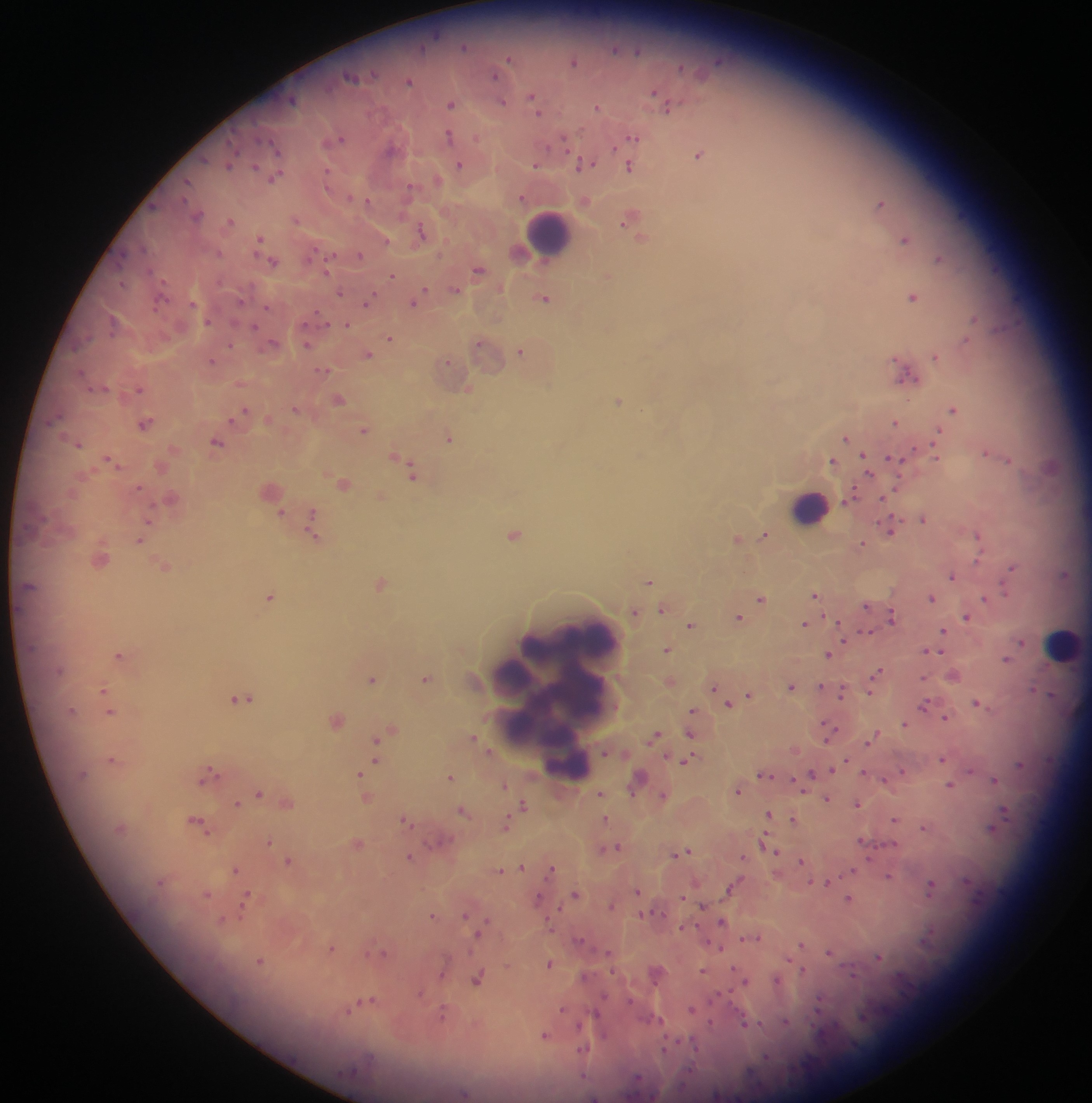

Approximate centers as {x, y} in pixels.
Summary:
  - Leukocyte locations: {549, 231}, {810, 505}, {570, 637}, {1062, 644}, {510, 680}, {559, 701}, {577, 702}, {567, 766}
  - Plasmodium parasite locations: {463, 46}, {615, 50}, {638, 51}, {509, 58}, {573, 61}, {718, 61}, {681, 67}, {495, 75}, {352, 77}, {409, 81}, {655, 92}, {533, 96}, {292, 100}, {501, 102}, {450, 104}, {597, 106}, {668, 106}, {538, 112}, {449, 136}, {632, 137}, {339, 139}, {477, 139}, {563, 141}, {276, 148}, {390, 149}, {698, 155}, {585, 164}, {228, 165}, {459, 165}, {536, 165}, {255, 167}, {630, 167}, {327, 175}, {275, 178}, {437, 180}, {187, 182}, {409, 187}, {350, 197}, {521, 197}, {367, 201}, {881, 203}, {153, 207}, {198, 215}, {630, 219}, {296, 220}, {230, 221}, {421, 231}, {642, 238}, {259, 239}, {904, 239}, {386, 240}, {143, 246}, {218, 253}, {360, 255}, {121, 258}, {939, 259}, {272, 261}, {327, 269}, {478, 270}, {392, 276}, {608, 277}, {122, 284}, {455, 290}, {340, 292}, {419, 295}, {912, 296}, {545, 298}, {240, 301}, {367, 302}, {415, 303}, {192, 304}, {266, 307}, {320, 317}, {974, 318}, {112, 321}, {208, 322}, {346, 324}, {255, 327}, {390, 339}, {965, 341}, {273, 343}, {478, 343}, {230, 345}, {306, 345}, {521, 351}, {367, 355}, {935, 357}, {211, 361}, {447, 362}, {323, 370}, {907, 376}, {468, 388}, {139, 389}, {339, 399}, {618, 401}, {296, 409}, {953, 409}, {244, 411}, {239, 415}, {54, 419}, {896, 422}, {145, 424}, {364, 430}, {937, 433}, {847, 437}, {449, 439}, {217, 442}, {78, 443}, {986, 452}, {937, 455}, {894, 458}, {866, 459}, {1009, 459}, {832, 460}, {112, 462}, {869, 471}, {412, 473}, {343, 484}, {138, 488}, {852, 495}, {883, 498}, {280, 514}, {311, 518}, {148, 519}, {924, 519}, {891, 529}, {313, 533}, {514, 534}, {765, 534}, {978, 535}, {737, 539}, {140, 540}, {862, 544}, {979, 558}, {165, 567}, {1011, 568}, {1064, 574}, {952, 576}, {649, 581}, {380, 583}, {1005, 592}, {816, 594}, {269, 597}, {931, 597}, {985, 598}, {761, 599}, {867, 605}, {663, 609}, {635, 613}, {891, 616}, {739, 617}, {966, 617}, {804, 624}, {690, 625}, {942, 631}, {866, 632}, {844, 638}, {1021, 642}, {667, 650}, {926, 652}, {941, 653}, {829, 654}, {119, 655}, {1006, 659}, {877, 672}, {372, 679}, {425, 679}, {924, 679}, {820, 686}, {792, 687}, {713, 688}, {1033, 688}, {843, 690}, {103, 691}, {870, 691}, {749, 695}, {243, 698}, {976, 702}, {728, 703}, {924, 705}, {692, 711}, {110, 713}, {946, 718}, {336, 720}, {904, 724}, {828, 729}, {391, 731}, {383, 734}, {691, 734}, {655, 736}, {473, 737}, {875, 737}, {375, 740}, {870, 742}, {111, 759}, {942, 759}, {685, 761}, {375, 762}, {846, 762}, {1020, 764}, {834, 770}, {902, 771}, {970, 771}, {865, 772}, {208, 774}, {360, 774}, {812, 774}, {762, 775}, {450, 777}, {638, 778}, {884, 780}, {995, 780}, {504, 785}, {950, 785}, {738, 790}, {258, 793}, {601, 794}, {664, 796}, {827, 799}, {857, 803}, {236, 804}, {287, 804}, {524, 805}, {464, 811}, {1005, 811}, {768, 814}, {605, 819}, {793, 820}, {895, 820}, {406, 821}, {198, 823}, {505, 826}, {924, 828}, {991, 828}, {861, 840}, {441, 841}, {269, 842}, {764, 843}, {358, 844}, {617, 847}, {769, 848}, {777, 851}, {686, 852}, {677, 854}, {408, 857}, {744, 857}, {801, 860}, {289, 861}, {522, 867}, {235, 869}, {551, 870}, {853, 870}, {500, 871}, {889, 876}, {828, 882}, {733, 886}, {931, 886}, {638, 891}, {575, 893}, {207, 895}, {682, 898}, {849, 899}, {537, 900}, {245, 903}, {612, 905}, {703, 907}, {640, 914}, {465, 915}, {432, 916}, {222, 920}, {722, 921}, {683, 928}, {480, 931}, {758, 938}, {579, 939}, {801, 945}, {332, 948}, {720, 948}, {829, 952}, {382, 954}, {608, 954}, {879, 957}, {260, 962}, {549, 963}, {443, 970}, {735, 970}, {802, 970}, {703, 971}, {478, 979}, {745, 980}, {777, 980}, {420, 994}, {603, 997}, {630, 1000}, {367, 1001}, {818, 1006}, {351, 1009}, {562, 1010}, {691, 1010}, {442, 1015}, {660, 1020}, {785, 1022}, {745, 1023}, {581, 1024}, {712, 1024}, {544, 1035}, {665, 1048}, {583, 1049}, {766, 1056}, {464, 1093}
  - Preparation: thick blood film
  - Country: Ghana
  - Field of view: single
  - Image size: 1092×1103 pixels
  - Capture: mobile-phone photograph through a microscope